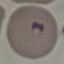
Malaria status: parasitized. Acquired by smartphone through the microscope eyepiece. Automatically extracted cell patch, resized to 64 × 64 pixels. Thin smear of blood. Giemsa-stained preparation.